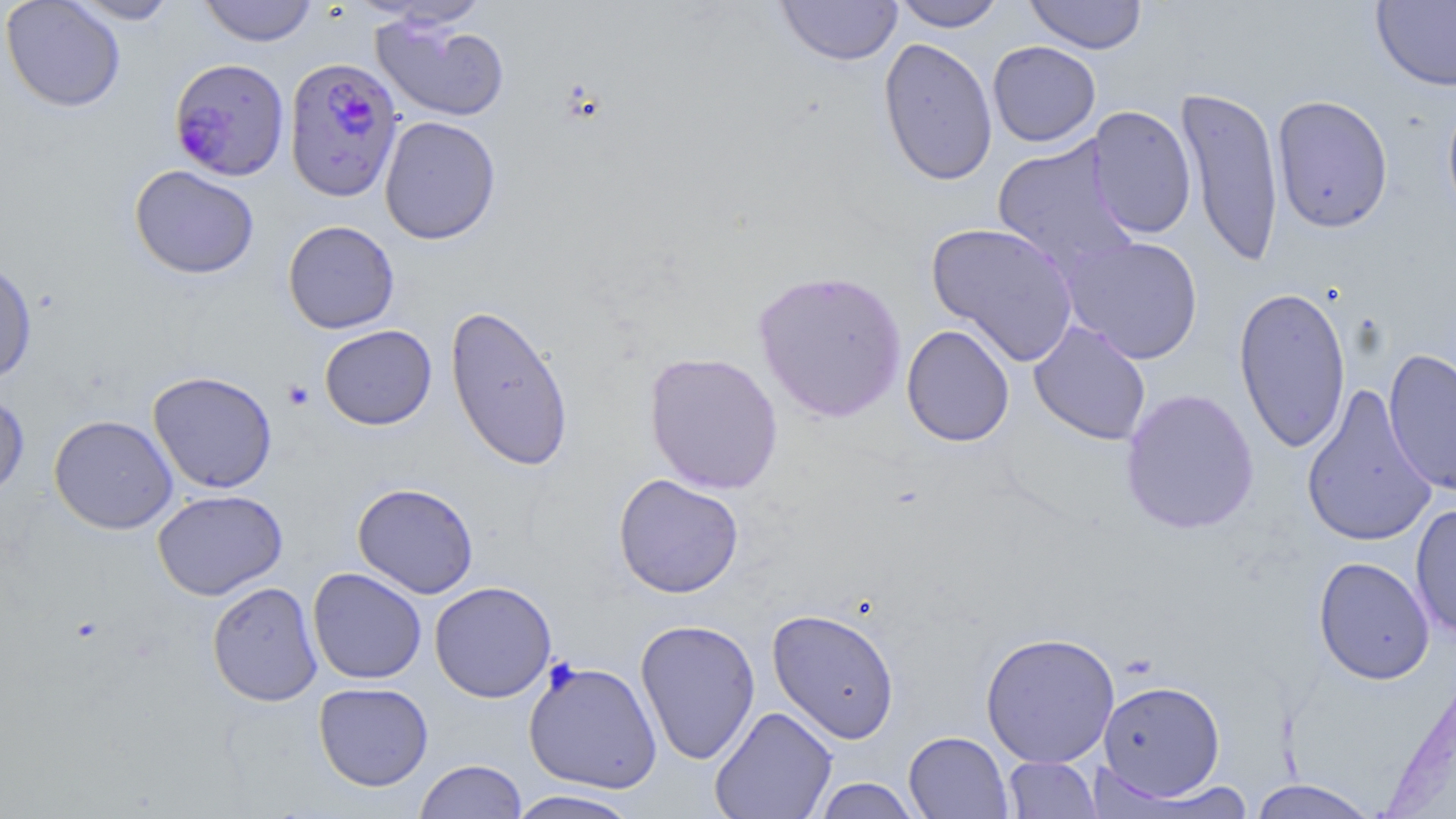
Approximate bounding boxes as (x1, y1, x2, y2) in pixels. Platelet locations: (283, 380, 313, 410). Plasmodium falciparum-infected red blood cell locations: (169, 57, 290, 181), (283, 57, 403, 202). Uninfected red blood cell locations: (1, 0, 126, 113), (68, 0, 181, 24), (198, 0, 319, 47), (775, 0, 903, 66), (892, 0, 1006, 31), (1025, 0, 1147, 54), (1371, 0, 1456, 92), (371, 14, 510, 122), (878, 36, 998, 187), (987, 41, 1101, 147), (1175, 85, 1284, 268), (1441, 89, 1456, 227), (1271, 94, 1394, 234), (1086, 105, 1197, 240), (379, 115, 501, 245), (992, 136, 1139, 277), (129, 165, 259, 279), (283, 220, 400, 334), (926, 221, 1080, 366), (1061, 235, 1204, 364), (0, 260, 37, 385), (753, 269, 907, 423), (1233, 285, 1352, 454), (445, 303, 574, 472), (1029, 321, 1151, 445), (319, 324, 437, 430), (901, 324, 1015, 447), (1384, 347, 1456, 498), (644, 351, 784, 494), (148, 371, 278, 494), (1301, 384, 1437, 548), (1120, 388, 1259, 535), (0, 389, 29, 501), (49, 414, 178, 534), (613, 473, 744, 598), (352, 482, 478, 598), (152, 489, 288, 600), (1410, 503, 1456, 640), (1313, 556, 1435, 685), (307, 567, 427, 684), (206, 580, 323, 706), (429, 581, 557, 703), (767, 608, 900, 743), (635, 618, 761, 765), (980, 631, 1120, 768), (523, 660, 662, 793), (1098, 679, 1225, 800), (313, 681, 433, 791), (709, 705, 837, 819), (903, 731, 1014, 819), (1002, 756, 1103, 818), (414, 759, 527, 819), (811, 778, 924, 818), (1247, 779, 1380, 818), (1130, 780, 1258, 818), (505, 789, 644, 818). Slide-level diagnosis: Plasmodium falciparum. Image is 1456×819 pixels. Captured at 1000x magnification. May-Grünwald-Giemsa stain. Single field of view. Light microscopy. Thin blood film.